Evaluate for malaria.
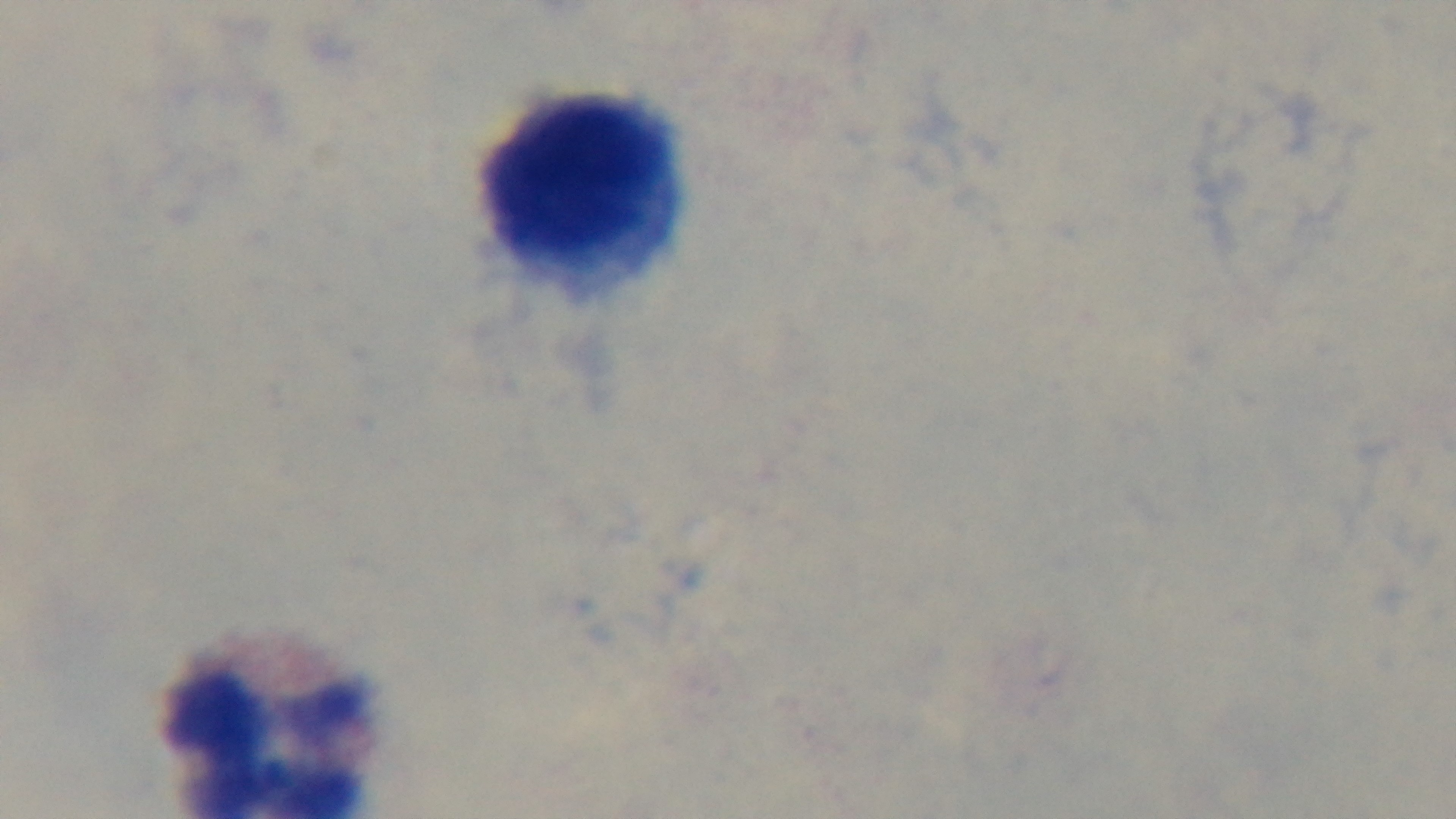
Negative.

Summary:
  - Preparation: thick
  - Stain: Giemsa
  - Capture: mounted 4K digital camera
  - Objective: 100x oil immersion
  - Modality: light microscopy
  - Field of view: single